Identify the parasite.
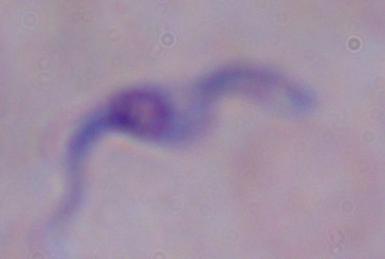

This is a trypanosome.

1000x magnification. Micrograph.